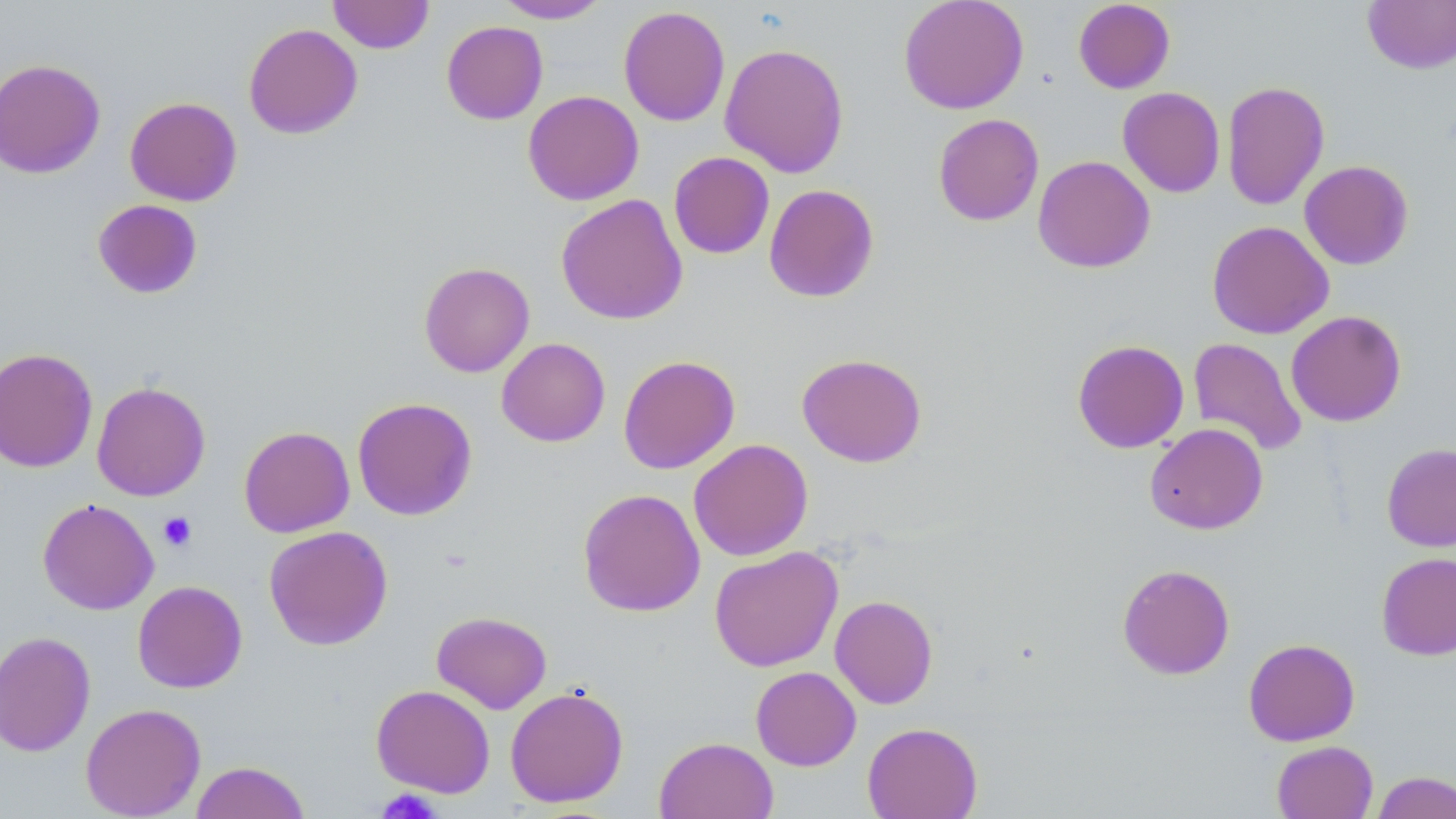

slide-level diagnosis = negative for blood parasites
magnification = 1000x
field of view = one of a larger specimen
image size = 1456×819 pixels
uninfected red blood cell locations = approximate bounding boxes as (x1, y1, x2, y2) in pixels: (328, 0, 434, 53), (898, 0, 1029, 115), (1073, 0, 1175, 94), (1362, 0, 1456, 74), (494, 1, 610, 23), (618, 5, 730, 127), (441, 21, 548, 125), (243, 23, 363, 139), (719, 42, 850, 178), (0, 58, 106, 179), (1222, 80, 1330, 210), (1118, 87, 1225, 197), (522, 90, 644, 205), (125, 96, 242, 206), (933, 113, 1044, 226), (669, 152, 775, 259), (1033, 155, 1155, 273), (1299, 160, 1414, 270), (764, 184, 879, 302), (556, 194, 688, 325), (92, 198, 203, 299), (1206, 220, 1334, 339), (418, 262, 535, 377), (1286, 310, 1406, 426), (496, 337, 610, 447), (1188, 337, 1308, 456), (1072, 339, 1189, 453), (0, 348, 98, 472), (797, 353, 927, 467), (618, 355, 740, 474), (91, 381, 211, 501), (352, 397, 477, 521), (1145, 423, 1268, 535), (238, 425, 355, 538), (688, 439, 813, 561), (1381, 443, 1456, 551), (577, 488, 705, 617), (37, 498, 159, 615), (264, 525, 393, 651), (709, 546, 843, 672), (1376, 552, 1456, 660), (1117, 563, 1235, 680), (132, 580, 248, 693), (830, 595, 938, 709), (431, 611, 552, 714), (0, 630, 96, 757), (1243, 638, 1360, 746), (751, 666, 861, 771), (371, 684, 495, 798), (505, 685, 629, 808), (80, 702, 206, 818), (862, 722, 982, 819), (654, 736, 778, 819), (1272, 741, 1378, 819), (190, 761, 309, 819), (1371, 771, 1456, 819)
stain = May-Grünwald-Giemsa
platelet locations = approximate bounding boxes as (x1, y1, x2, y2) in pixels: (158, 512, 197, 552), (378, 787, 439, 819)
modality = optical microscopy
preparation = thin blood film